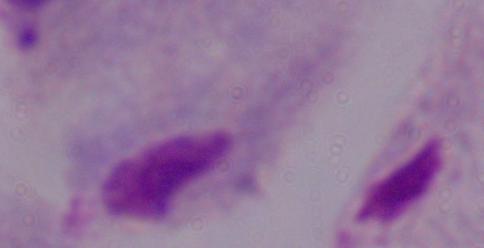 1000x magnification. Micrograph. A trichomonad is shown.